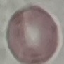
Malaria status: uninfected. Thin blood smear. Giemsa-stained preparation. Photographed with a smartphone camera at the microscope eyepiece. Cell patch, automatically extracted from a larger field of view and resized to 64 × 64 pixels.